Identify the parasite.
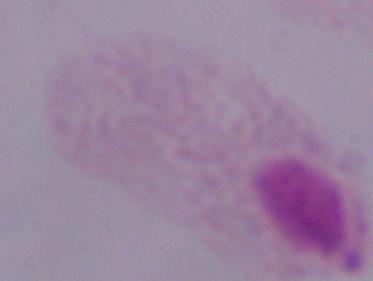
A trichomonad.

modality: micrograph
magnification: 1000x